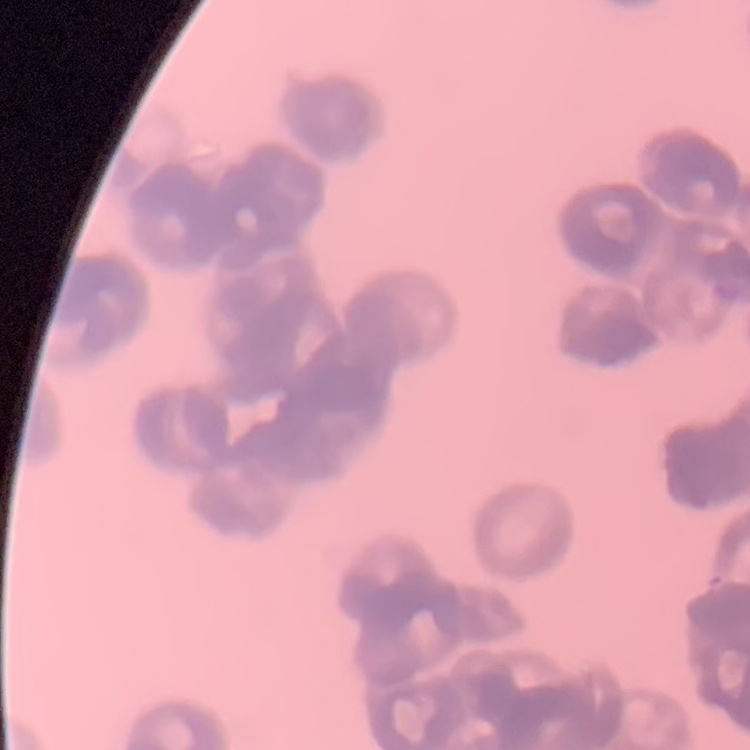
The red blood cells show rouleaux formation. Field's or Giemsa stain. Square crop of a larger photomicrograph. Thin blood smear.